State which parasite is depicted.
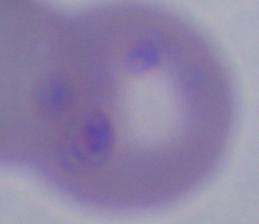

Babesia.

Summary:
  - Magnification: 1000x
  - Modality: micrograph